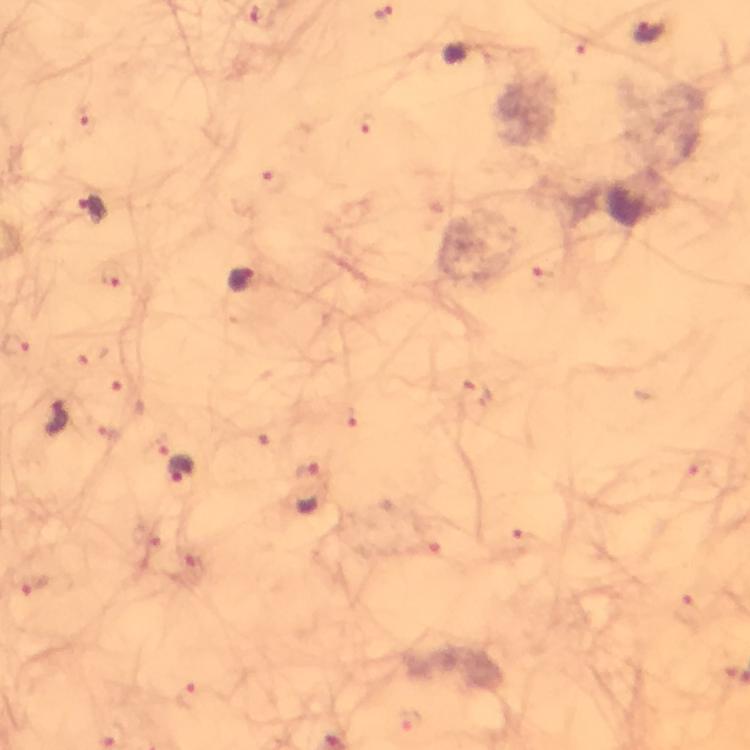
stain = Giemsa
context = from a malaria diagnostic workup
image size = 750×750 pixels
capture = smartphone mounted on the microscope
magnification = 100x
immersion oil = applied
Plasmodium parasite locations = approximate centers as (x, y) in pixels: (384, 12), (649, 32), (92, 208), (241, 283), (56, 419), (180, 471), (309, 489), (33, 586)
cropped from = one field of view
preparation = thick smear